Name the parasite shown.
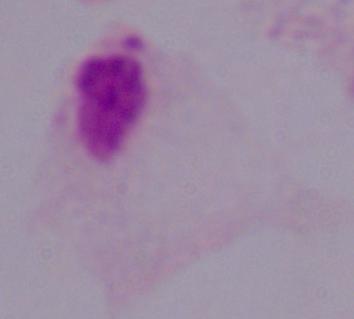

This is a trichomonad.

1000x magnification. Photomicrograph.